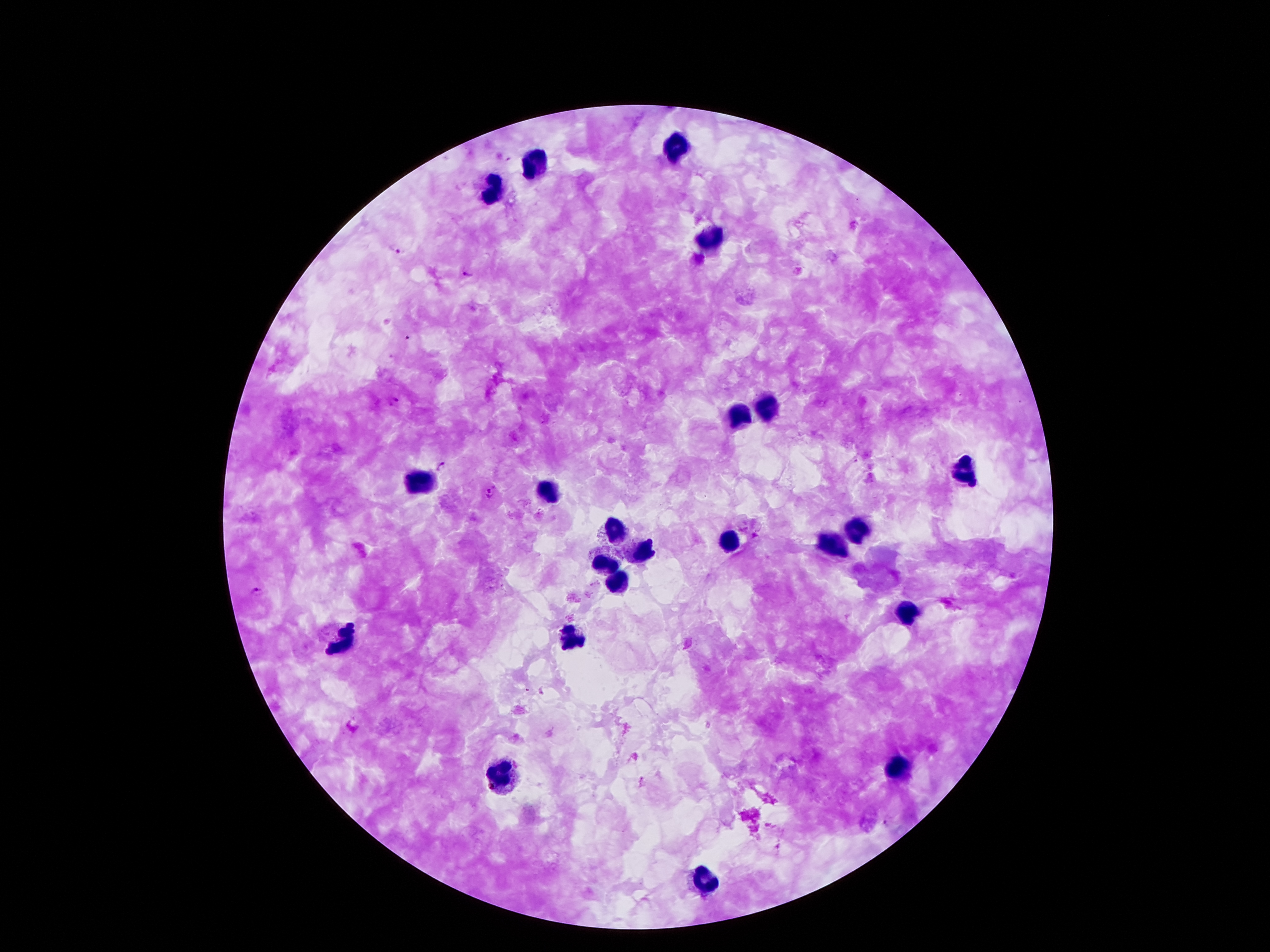
Approximate centers as [x, y] in pixels. Plasmodium parasite locations: [397, 249], [466, 272], [410, 335], [397, 400], [441, 465], [489, 493], [257, 590], [887, 823]. Leukocyte locations: [679, 145], [534, 160], [492, 187], [709, 243], [772, 404], [742, 415], [966, 472], [417, 474], [546, 492], [618, 526], [858, 528], [726, 539], [837, 545], [637, 550], [606, 560], [616, 581], [908, 611], [571, 636], [350, 637], [900, 769], [501, 775], [709, 882]. Patient malaria status: positive for Plasmodium falciparum. 100x magnification. Thick peripheral-blood smear. Smartphone photograph taken through the microscope eyepiece. One field from this slide. Giemsa stain. Image is 1270×952 pixels.